Comment on the morphology of the red blood cells.
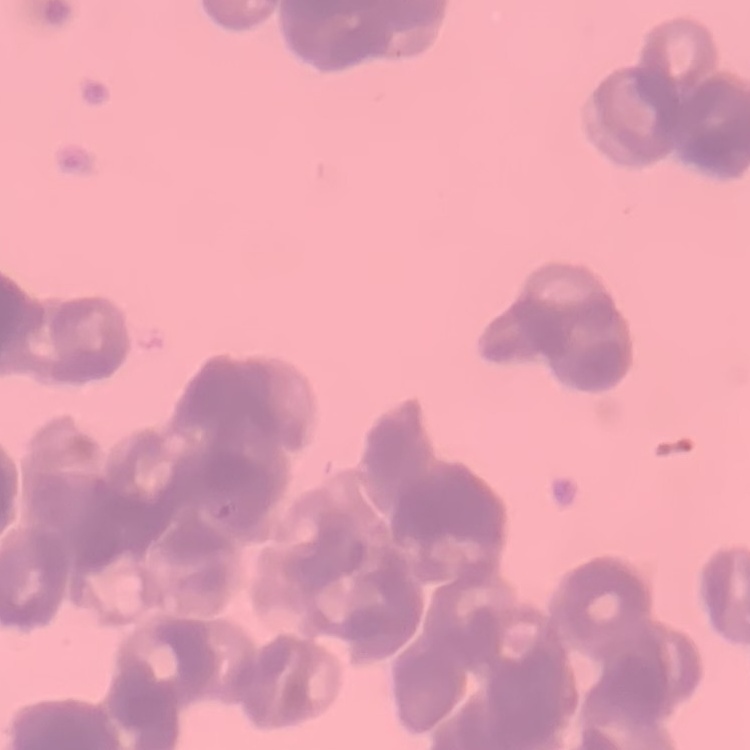
Rouleaux formation.

{
  "image_type": "square crop of a larger photomicrograph",
  "preparation": "thin blood film",
  "stain": "Field's or Giemsa"
}